Comment on the morphology of the erythrocytes.
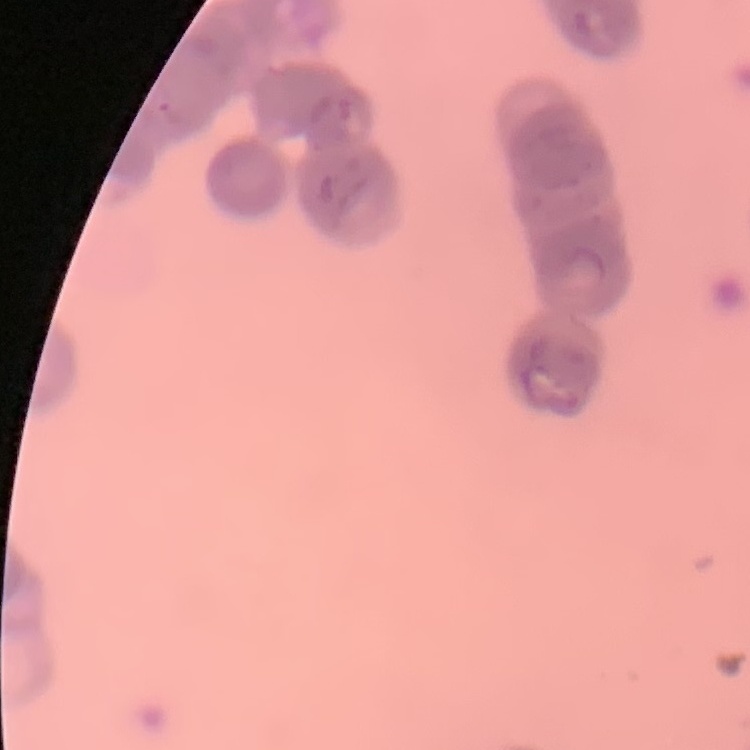
They show rouleaux formation.

Thin peripheral smear. One tile cut from a larger photomicrograph. Field's or Giemsa stain.